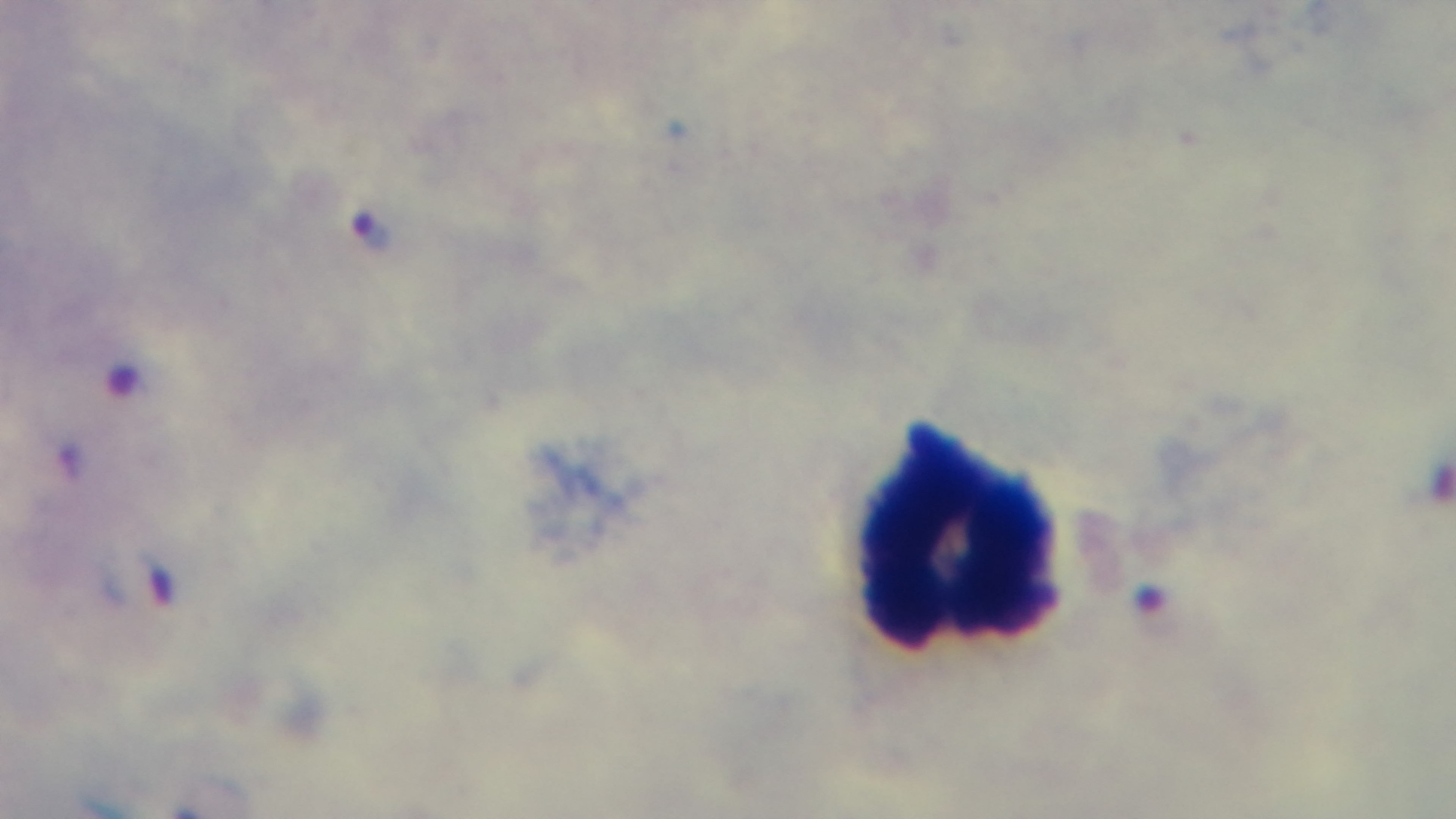

Summary:
  - Preparation: thick blood film
  - Malaria status: infected
  - Field of view: single
  - Stain: Giemsa
  - Modality: light microscopy
  - Capture: mounted 4K digital camera
  - Objective: 100x oil immersion